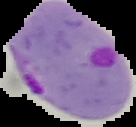

result = Plasmodium parasites identified
image size = 136×127 pixels
preparation = thin blood smear
image type = cell region segmented out of the field of view; surrounding area masked to black